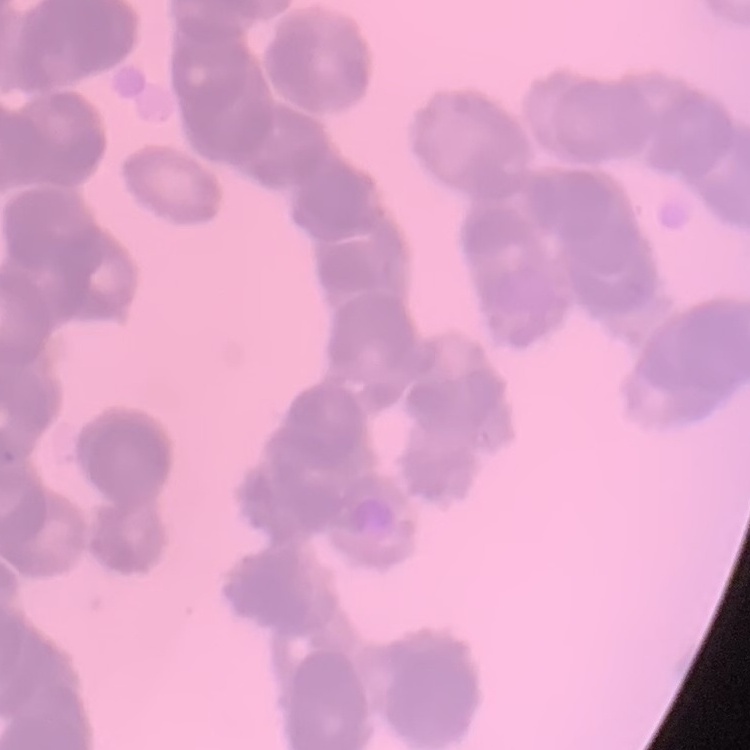
Summary:
  - Erythrocyte morphology: rouleaux formation
  - Preparation: thin blood smear
  - Image type: square crop of a larger photomicrograph
  - Stain: Field's or Giemsa